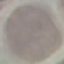

malaria status = uninfected
preparation = thin blood smear
image type = cell patch, automatically extracted from a larger field of view and resized to 64 × 64 pixels
capture = smartphone camera at the microscope eyepiece
stain = Giemsa